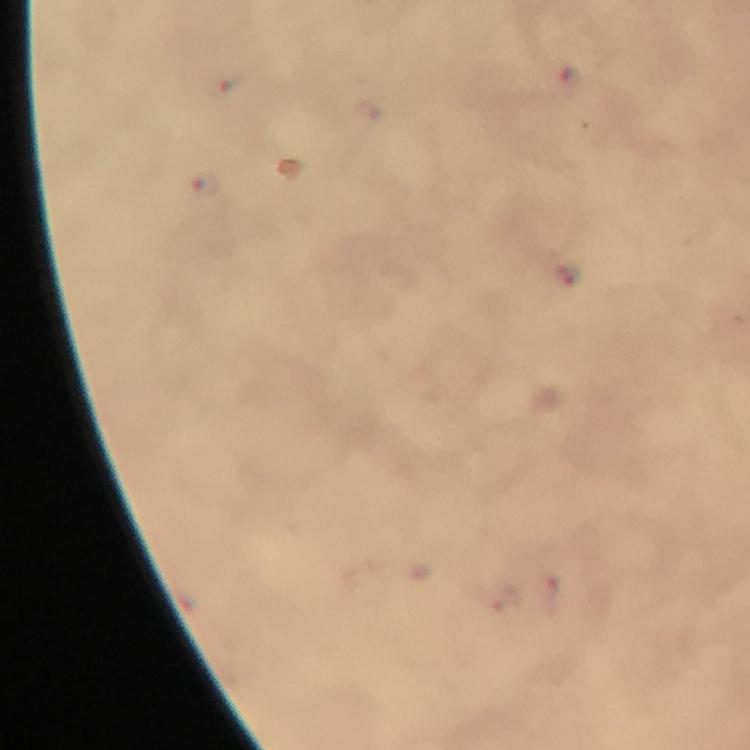

image size = 750×750 pixels
stain = Giemsa
capture = smartphone camera through the microscope
magnification = 100x
malaria parasite locations = approximate centers as [x, y] in pixels: [569, 80], [203, 184], [566, 275]
preparation = thick smear
cropped from = one field of view
context = from a malaria diagnostic workup
immersion oil = applied